Evaluate for malaria.
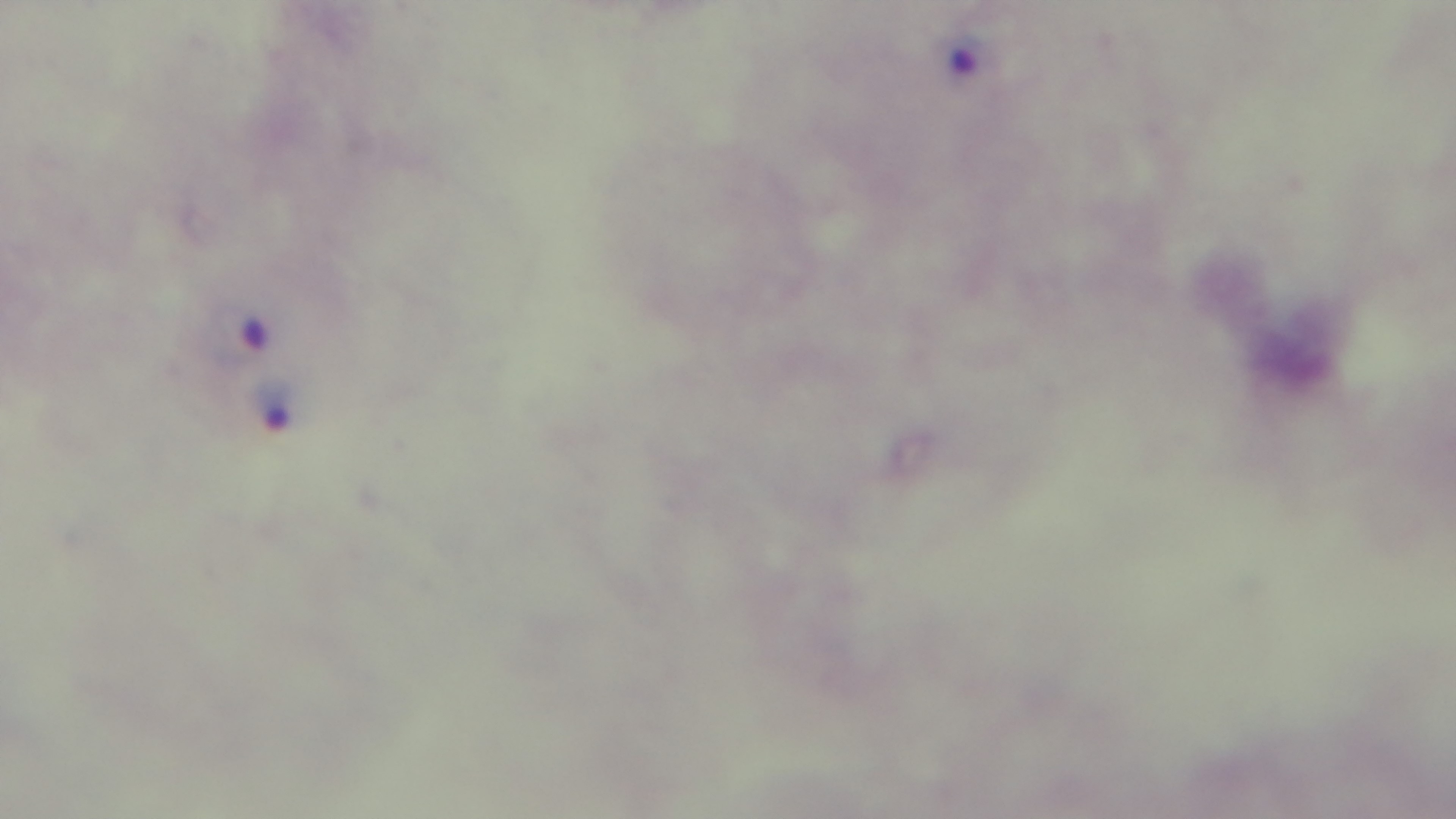

Infected.

Summary:
  - Field of view: single
  - Stain: Giemsa
  - Objective: 100x oil immersion
  - Modality: light microscopy
  - Capture: mounted 4K digital camera
  - Preparation: thick blood film